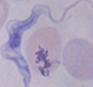
Summary:
  - Magnification: 1000x
  - Identification: trypanosome
  - Modality: photomicrograph